Locate every Plasmodium vivax-infected red blood cell.
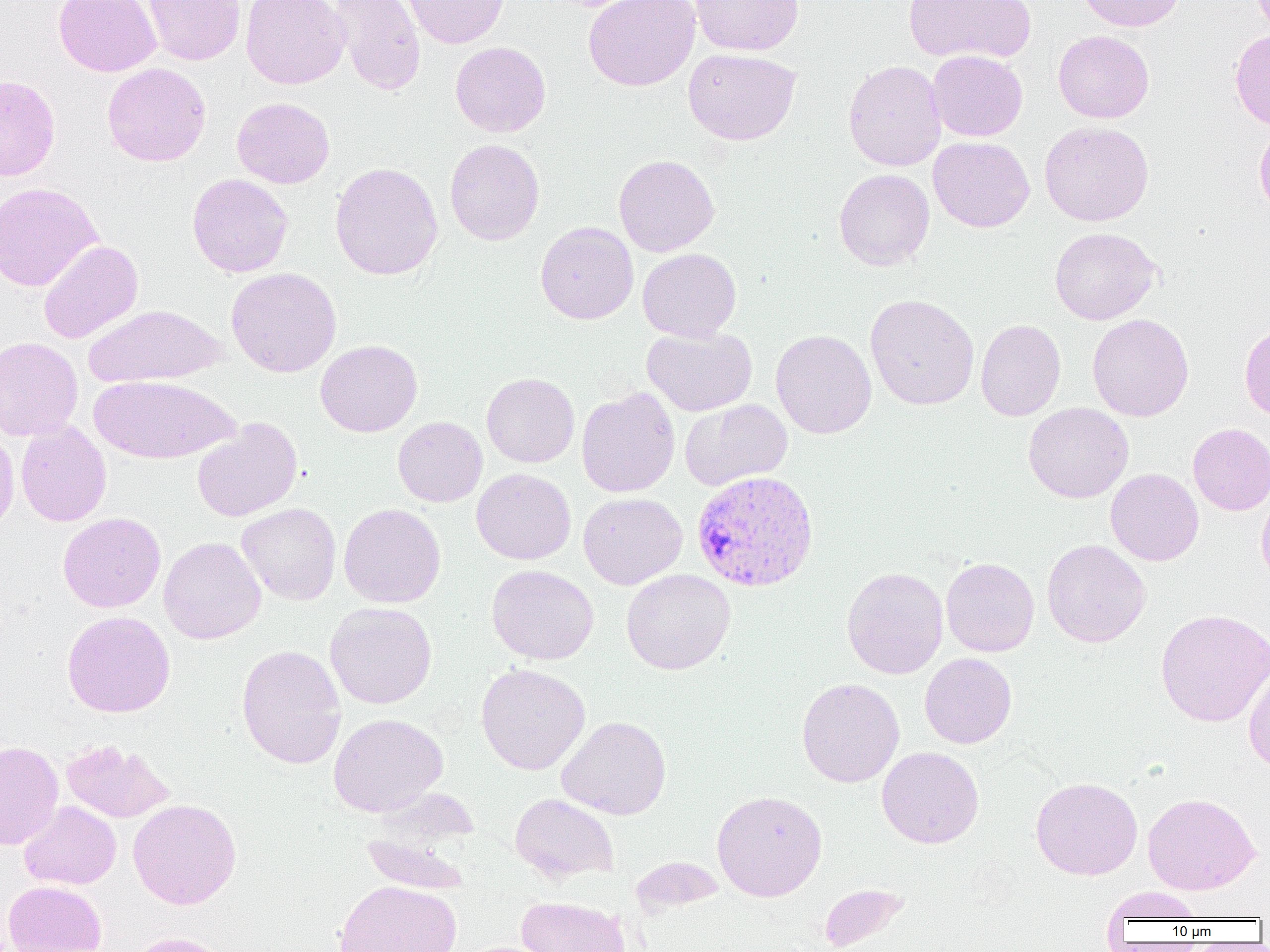

Approximate bounding boxes as [x1, y1, x2, y2] in pixels.
Plasmodium vivax-infected red blood cells: [691, 470, 820, 593].

slide-level diagnosis = Plasmodium vivax
magnification = 1000x
uninfected red blood cell locations = approximate bounding boxes as [x1, y1, x2, y2] in pixels: [53, 0, 161, 77], [143, 0, 245, 65], [241, 0, 350, 89], [328, 0, 426, 96], [396, 0, 509, 49], [583, 0, 700, 91], [690, 0, 804, 56], [903, 0, 1037, 64], [1077, 0, 1185, 31], [1053, 30, 1154, 123], [1230, 30, 1270, 130], [450, 41, 551, 137], [683, 48, 801, 145], [927, 50, 1027, 141], [843, 59, 947, 171], [102, 63, 211, 166], [0, 74, 60, 181], [232, 97, 335, 188], [1254, 120, 1270, 219], [1039, 121, 1154, 227], [928, 136, 1035, 232], [444, 138, 545, 245], [613, 154, 720, 257], [330, 162, 443, 281], [834, 169, 935, 271], [186, 173, 293, 277], [0, 182, 102, 292], [535, 222, 638, 324], [1050, 227, 1161, 325], [38, 240, 143, 344], [638, 248, 741, 342], [226, 267, 341, 377], [865, 294, 979, 410], [84, 304, 226, 387], [1087, 313, 1194, 421], [976, 319, 1065, 421], [1239, 321, 1270, 421], [642, 326, 757, 416], [770, 329, 877, 438], [0, 337, 83, 441], [315, 339, 423, 437], [481, 373, 580, 467], [89, 374, 240, 464], [576, 386, 680, 498], [680, 399, 793, 491], [1023, 402, 1134, 503], [393, 416, 487, 507], [192, 418, 302, 522], [15, 421, 112, 527], [1187, 423, 1270, 515], [0, 424, 20, 535], [472, 468, 576, 565], [1105, 468, 1204, 566], [1256, 485, 1270, 585], [578, 492, 688, 589], [236, 503, 341, 605], [339, 503, 446, 608], [58, 511, 166, 613], [158, 536, 266, 644], [1042, 539, 1151, 647], [940, 557, 1039, 657], [486, 564, 598, 665], [841, 567, 948, 679], [622, 569, 736, 674], [325, 602, 437, 709], [1155, 608, 1270, 727], [62, 611, 175, 717], [236, 644, 347, 769], [919, 653, 1017, 749], [1243, 661, 1270, 772], [475, 663, 591, 774], [796, 677, 904, 787], [328, 712, 448, 817], [557, 715, 671, 820], [61, 739, 174, 822], [0, 741, 63, 850], [877, 746, 984, 848], [1031, 776, 1143, 880], [712, 790, 827, 901], [1143, 792, 1260, 895], [511, 793, 619, 882], [128, 798, 242, 909], [19, 801, 121, 889], [361, 834, 471, 893], [631, 856, 723, 915], [335, 879, 460, 952], [2, 880, 107, 952], [819, 883, 909, 951], [1101, 887, 1208, 924], [516, 896, 632, 952], [125, 932, 234, 952]
field of view = single
preparation = thin blood smear
image size = 1270×952 pixels
modality = light microscopy